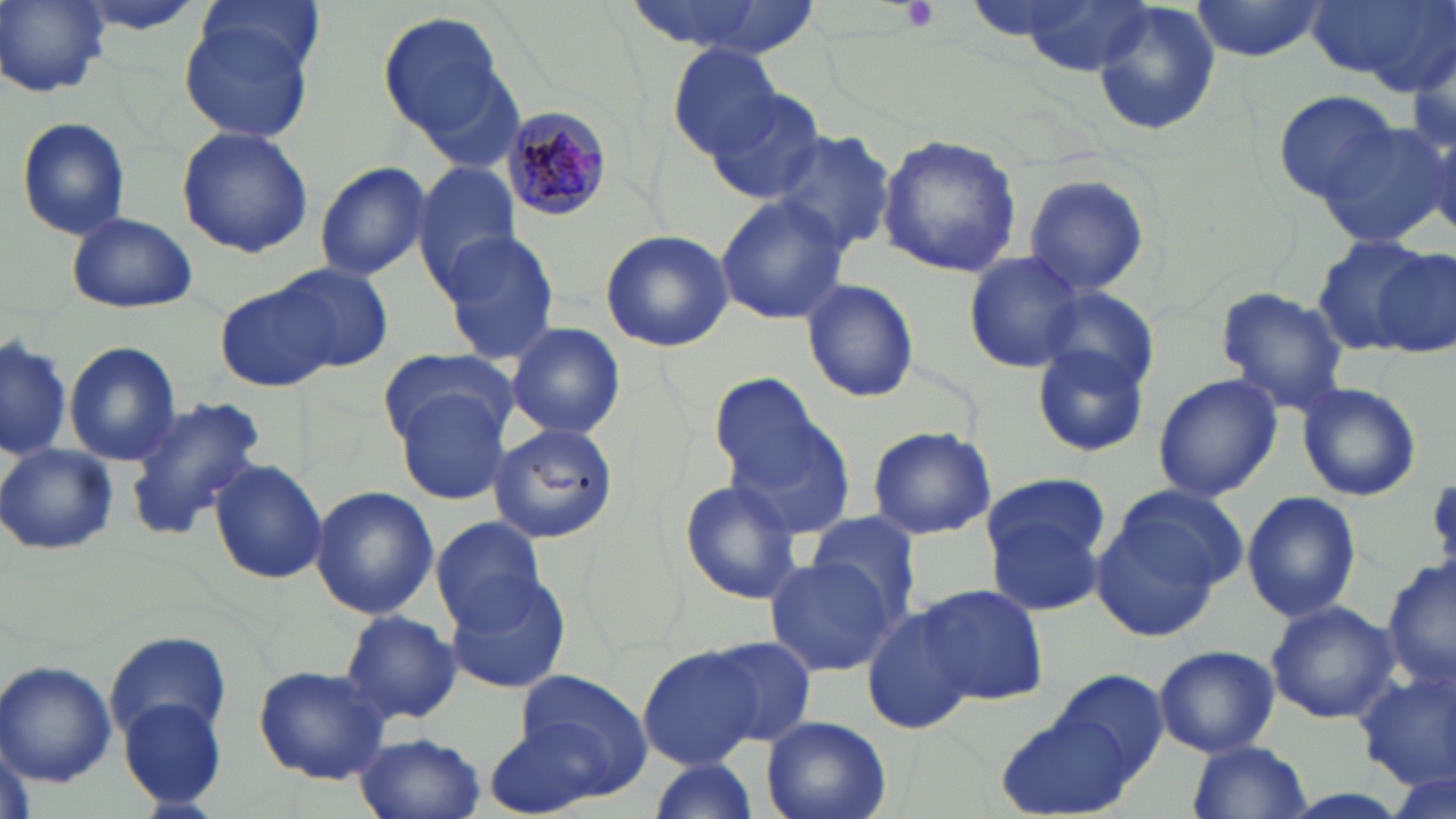
slide-level diagnosis = Plasmodium malariae
stain = May-Grünwald-Giemsa
Plasmodium malariae-infected red blood cell locations = approximate bounding boxes as (x1,y1)-(x2,y2) corner pairs in pixels: (502,106)-(614,221)
preparation = thin blood smear
image size = 1456×819 pixels
magnification = 1000x
uninfected red blood cell locations = approximate bounding boxes as (x1,y1)-(x2,y2) corner pairs in pixels: (2,0)-(109,97), (196,0)-(325,83), (625,0)-(820,60), (1186,0)-(1333,62), (1304,0)-(1452,88), (1000,1)-(1160,76), (1090,2)-(1218,137), (377,9)-(518,152), (179,12)-(321,143), (1408,36)-(1456,160), (668,44)-(784,159), (703,89)-(827,207), (1274,89)-(1397,202), (16,116)-(131,241), (1317,124)-(1450,248), (177,125)-(313,258), (767,131)-(896,256), (877,134)-(1023,278), (412,161)-(520,287), (313,162)-(432,281), (1023,172)-(1149,297), (715,194)-(848,326), (65,212)-(198,314), (438,230)-(563,363), (599,230)-(734,353), (1311,234)-(1439,355), (1372,247)-(1455,354), (962,250)-(1088,374), (272,261)-(394,373), (801,280)-(920,402), (216,283)-(338,394), (1214,285)-(1351,412), (1039,289)-(1160,396), (505,322)-(626,440), (2,332)-(71,464), (1,335)-(74,460), (65,342)-(182,466), (1031,344)-(1150,458), (376,347)-(517,448), (710,374)-(853,533), (1153,374)-(1282,501), (387,381)-(515,504), (1295,381)-(1422,503), (125,397)-(267,540), (487,422)-(622,546), (866,425)-(996,539), (0,443)-(118,557), (208,458)-(329,585), (982,477)-(1113,619), (676,478)-(805,605), (308,487)-(439,619), (1089,489)-(1236,635), (1242,490)-(1361,623), (810,513)-(922,625), (430,516)-(549,633), (1385,556)-(1456,695), (764,558)-(893,677), (444,574)-(574,696), (917,584)-(1052,705), (1265,600)-(1398,723), (860,606)-(975,736), (336,610)-(462,725), (107,630)-(230,745), (700,636)-(817,747), (638,644)-(766,768), (1155,645)-(1280,756), (0,659)-(117,788), (1353,663)-(1456,789), (254,664)-(393,784), (1054,667)-(1169,781), (510,670)-(656,804), (117,697)-(229,812), (994,709)-(1138,819), (480,714)-(623,817), (760,715)-(891,819), (355,733)-(486,819), (1186,741)-(1313,818), (644,757)-(759,819)
platelet locations = approximate bounding boxes as (x1,y1)-(x2,y2) corner pairs in pixels: (901,0)-(941,32)
field of view = one of a larger specimen
modality = optical microscopy